Locate every Plasmodium parasite.
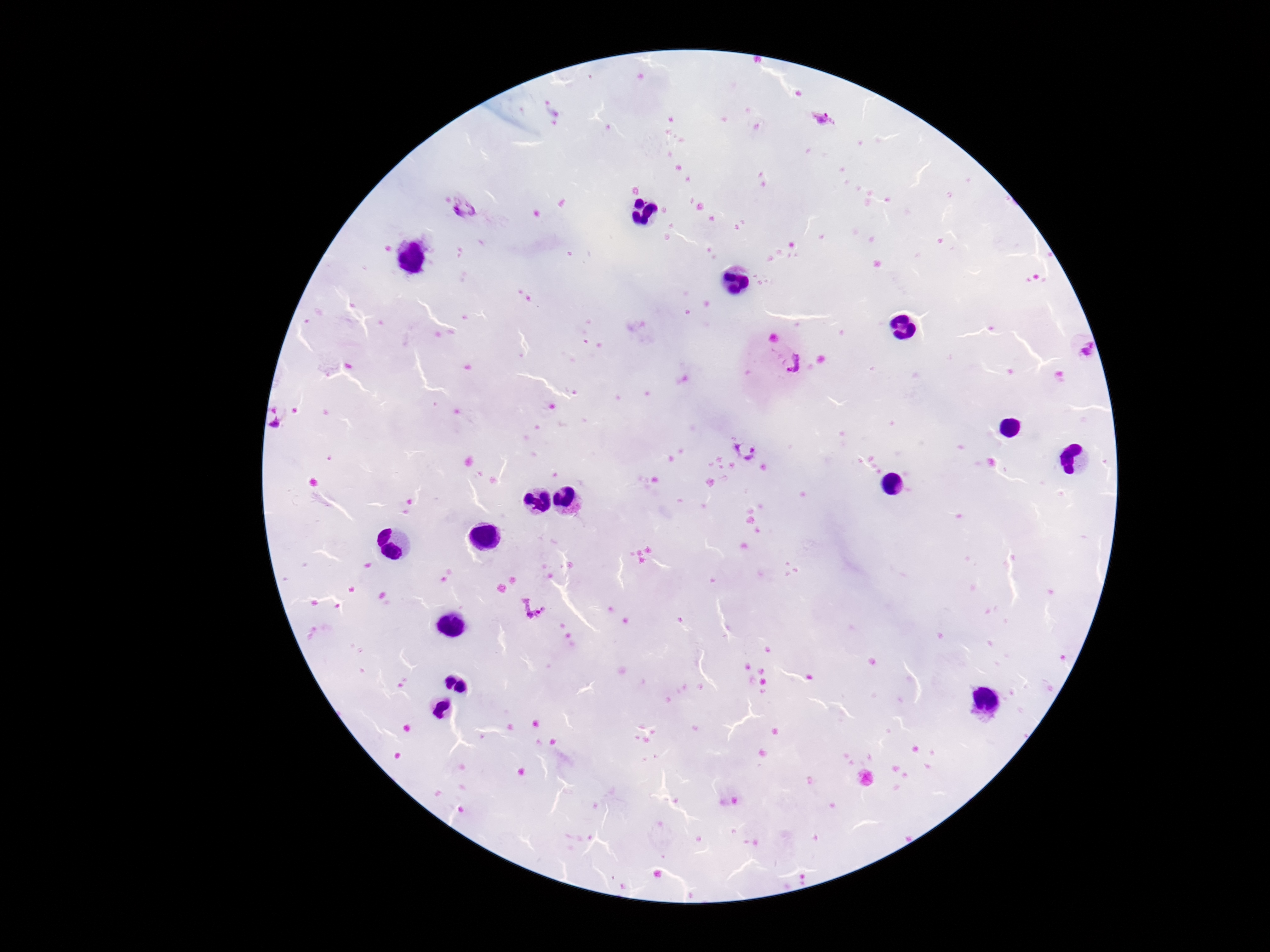

Approximate object centers, in pixels from the top-left corner.
Plasmodium parasites: (x=825, y=119), (x=462, y=207), (x=1079, y=352), (x=793, y=365), (x=283, y=412), (x=745, y=450), (x=534, y=606).

One field from this slide. Photographed through the microscope eyepiece with a smartphone camera. Image is 1270×952 pixels. Patient malaria status: positive. Thick blood film. 100x magnification. Giemsa-stained preparation.